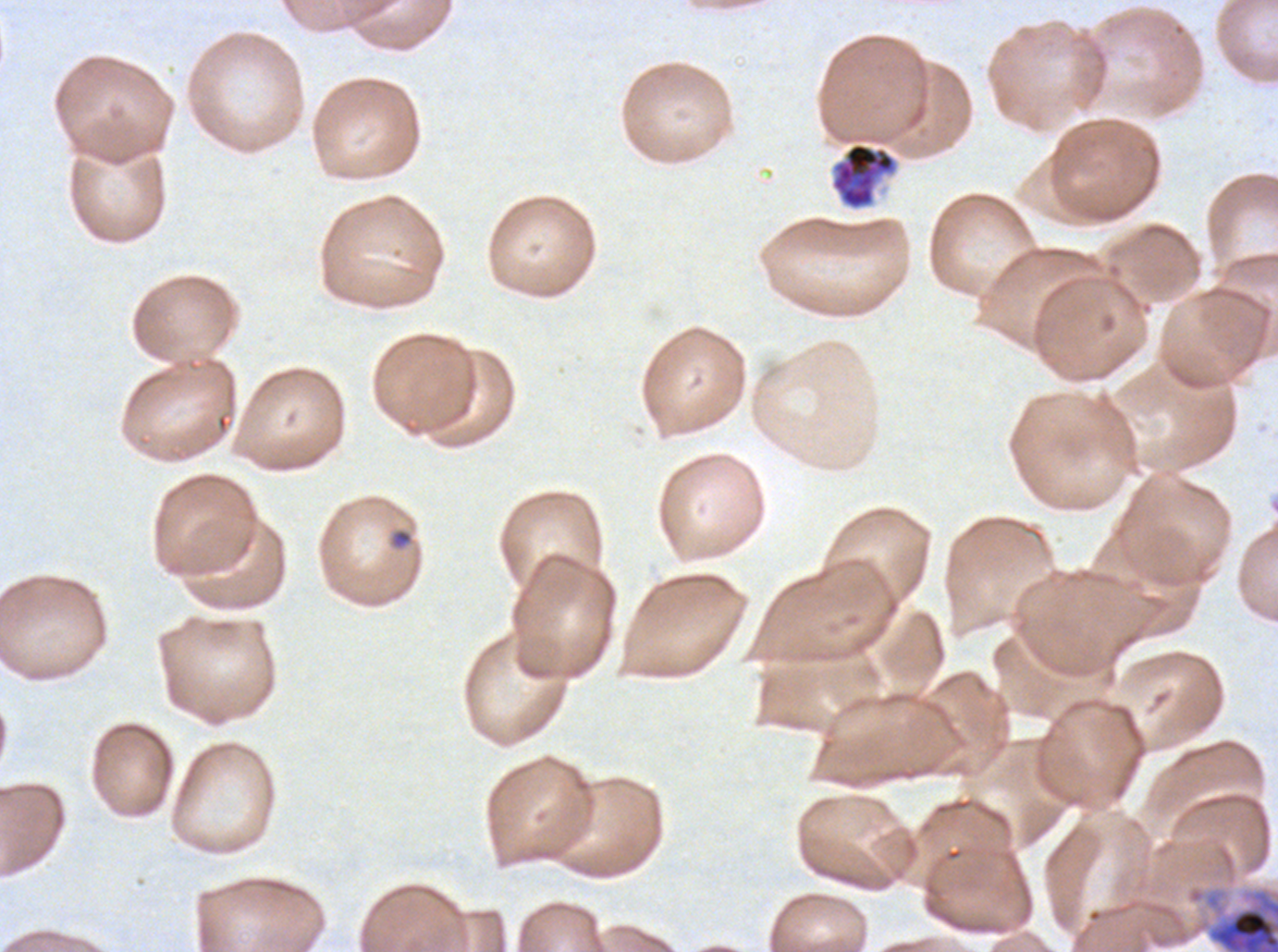 Approximate bounding boxes as (x1, y1, x2, y2) in pixels. Late schizont locations: (829, 141, 898, 211). Early schizont locations: (1186, 884, 1277, 951). Late-ring/early-trophozoite locations: (390, 529, 413, 549). A sub-image separated from a larger composite. Image is 1278×952 pixels. Life-cycle stages observed: late-ring/early-trophozoite, early schizont, late schizont. Giemsa-stained preparation. Ex-vivo Plasmodium falciparum culture from a patient in The Gambia, grown for 24 to 48 hours. Thin blood film.